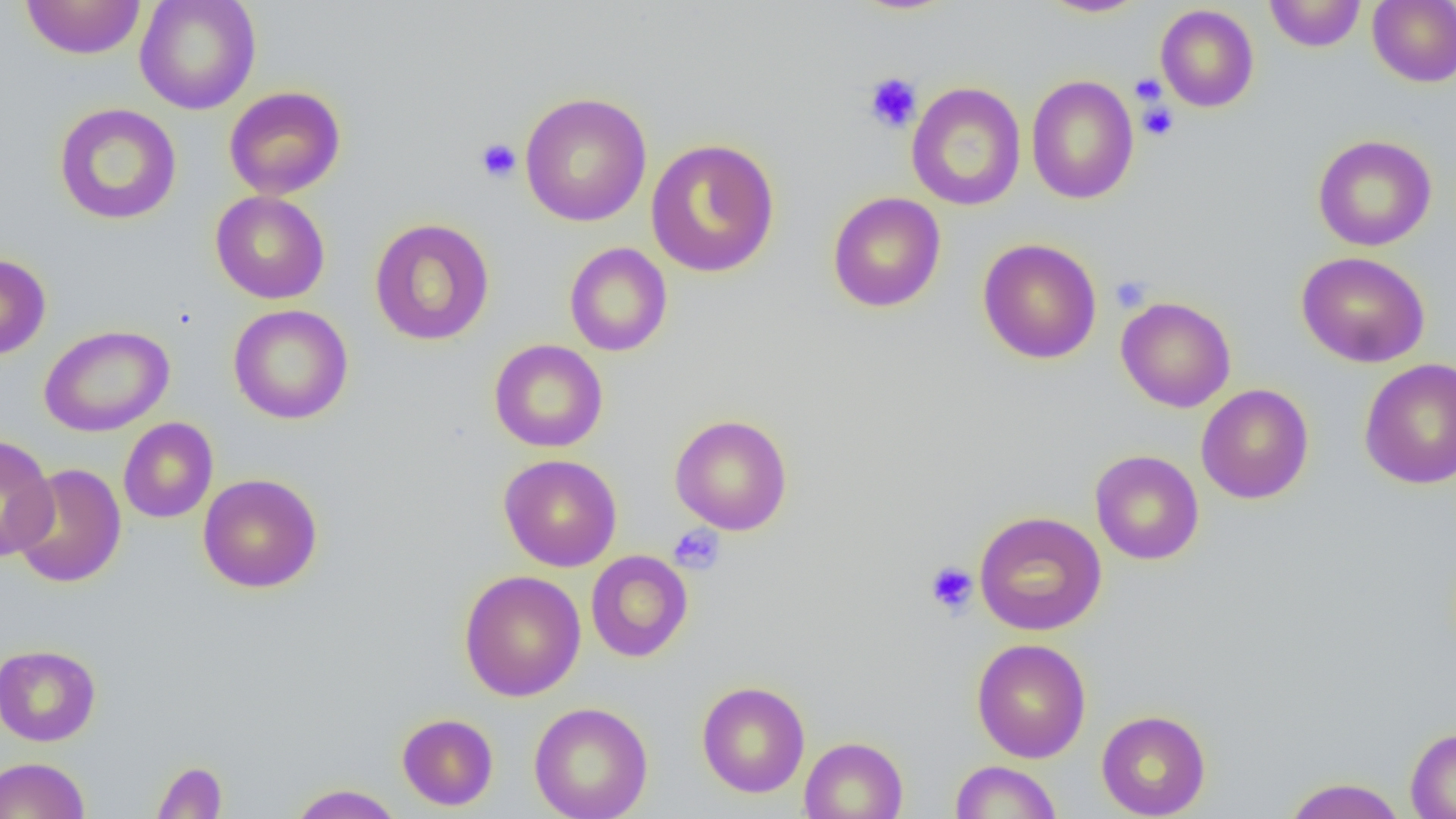
slide-level diagnosis = negative for blood parasites
platelet locations = approximate bounding boxes as (x1,y1)-(x2,y2) corner pairs in pixels: (864,72)-(922,133), (1129,74)-(1168,105), (1138,102)-(1179,140), (475,138)-(522,183), (1110,276)-(1151,312), (668,524)-(726,575), (924,561)-(978,615)
uninfected red blood cell locations = approximate bounding boxes as (x1,y1)-(x2,y2) corner pairs in pixels: (20,0)-(147,59), (135,0)-(261,114), (849,0)-(961,15), (1039,0)-(1150,18), (1264,0)-(1366,52), (1367,1)-(1456,87), (1155,4)-(1259,113), (1026,74)-(1139,205), (906,81)-(1027,212), (224,86)-(346,199), (519,91)-(652,226), (53,103)-(182,225), (1312,134)-(1437,251), (645,138)-(781,278), (210,190)-(330,304), (827,192)-(946,313), (369,218)-(495,346), (977,238)-(1102,364), (564,242)-(673,356), (1296,251)-(1431,368), (0,253)-(51,361), (1116,296)-(1236,412), (228,304)-(354,424), (40,324)-(174,437), (488,339)-(608,453), (1359,358)-(1456,489), (1196,384)-(1314,504), (669,414)-(793,535), (118,417)-(218,523), (0,435)-(58,562), (1089,449)-(1204,565), (498,454)-(622,571), (9,464)-(126,588), (198,473)-(323,593), (974,510)-(1106,635), (585,550)-(693,663), (458,569)-(586,701), (971,638)-(1091,763), (0,644)-(101,746), (697,681)-(810,798), (529,701)-(653,819), (1096,710)-(1211,819), (397,713)-(499,811), (1405,728)-(1456,818), (799,736)-(908,819), (0,757)-(90,819), (151,760)-(228,819), (950,760)-(1063,818), (1282,777)-(1407,819), (287,784)-(405,818)
preparation = thin blood smear
image size = 1456×819 pixels
field of view = single
magnification = 1000x
modality = optical microscopy